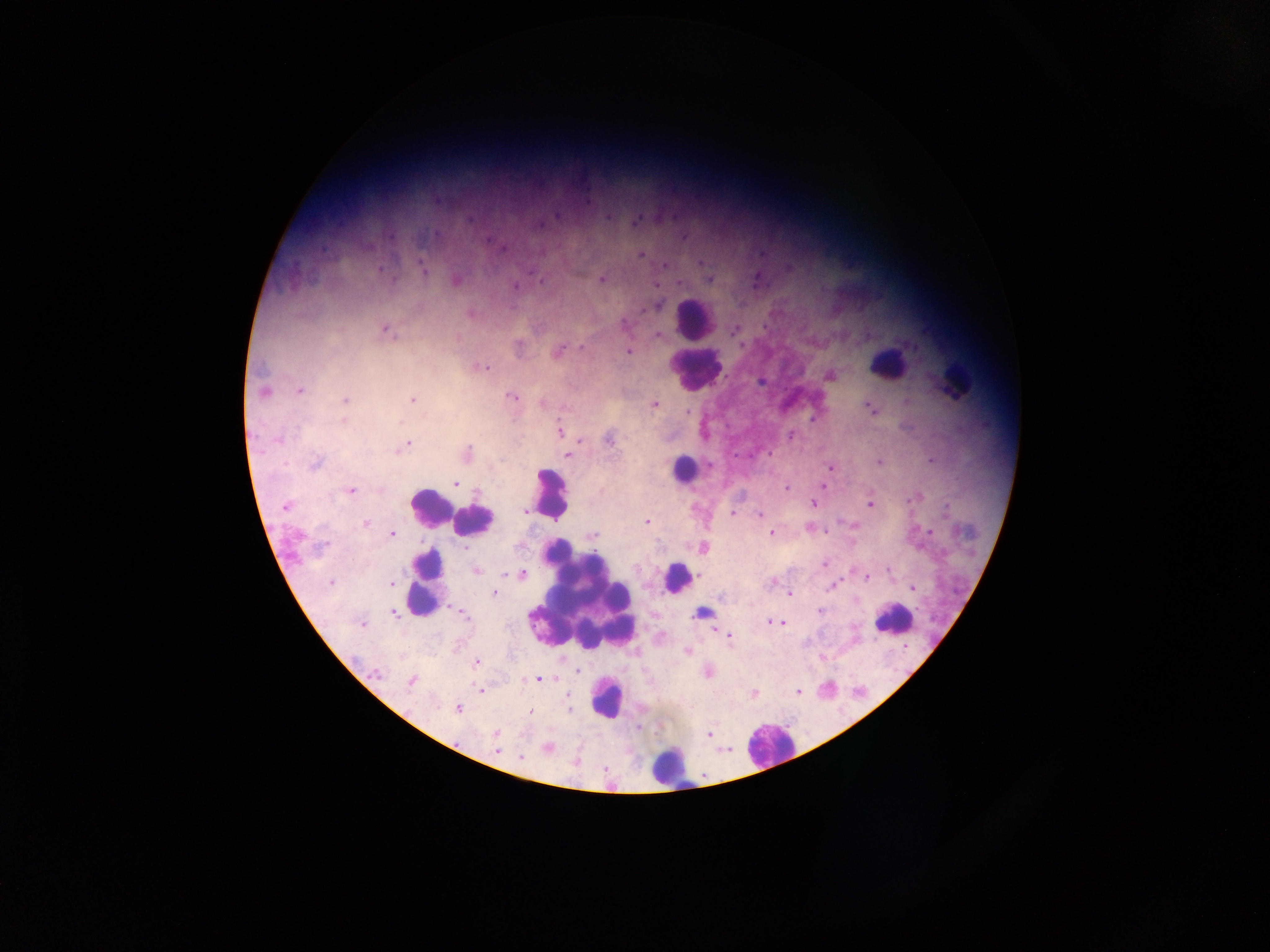

Approximate centers as [x, y] in pixels.
Summary:
  - Leukocyte locations: [695, 320], [888, 363], [696, 367], [953, 380], [683, 469], [550, 492], [429, 505], [449, 511], [474, 521], [677, 578], [426, 581], [583, 597], [893, 619], [607, 698], [768, 744], [668, 766]
  - Malaria parasite locations: [606, 218], [636, 222], [435, 234], [684, 236], [642, 254], [664, 265], [422, 267], [530, 273], [457, 279], [602, 279], [709, 279], [542, 281], [680, 283], [515, 286], [656, 306], [624, 325], [735, 329], [386, 331], [658, 335], [519, 345], [582, 348], [559, 350], [629, 352], [483, 367], [829, 375], [300, 389], [263, 390], [511, 397], [413, 399], [345, 400], [544, 402], [654, 405], [870, 409], [688, 411], [343, 420], [559, 431], [791, 434], [609, 439], [405, 446], [467, 453], [769, 453], [568, 454], [879, 462], [315, 463], [830, 467], [455, 483], [823, 485], [787, 488], [351, 491], [813, 504], [869, 505], [285, 507], [525, 511], [732, 514], [760, 514], [646, 522], [366, 524], [930, 531], [771, 533], [392, 534], [592, 535], [322, 546], [465, 547], [703, 547], [825, 564], [887, 570], [477, 571], [522, 573], [867, 578], [331, 583], [771, 583], [391, 584], [833, 586], [912, 588], [494, 594], [790, 594], [820, 612], [393, 613], [701, 613], [462, 614], [770, 621], [776, 623], [782, 623], [362, 624], [729, 636], [686, 652], [476, 662], [577, 671], [378, 674], [538, 679], [410, 683], [480, 690], [798, 691], [754, 694], [458, 708], [569, 709], [530, 712], [497, 733], [710, 734], [548, 748], [497, 750], [521, 759]
  - Country: Ghana
  - Image size: 1270×952 pixels
  - Preparation: thick blood smear
  - Capture: mobile-phone photograph through a microscope
  - Field of view: single